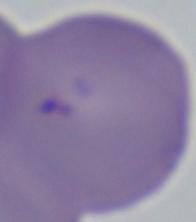

A Babesia parasite is shown. Photomicrograph. 1000x magnification.